Classify this cell by malaria status.
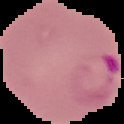
It is parasitized.

The area outside the segmented cell region is set to black. From a thin blood film. Image is 124×124 pixels.